Classify this cell by malaria status.
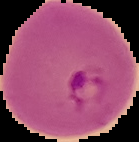
Parasitized.

Segmented cell region on a black background. Image is 139×142 pixels. From a thin blood smear.